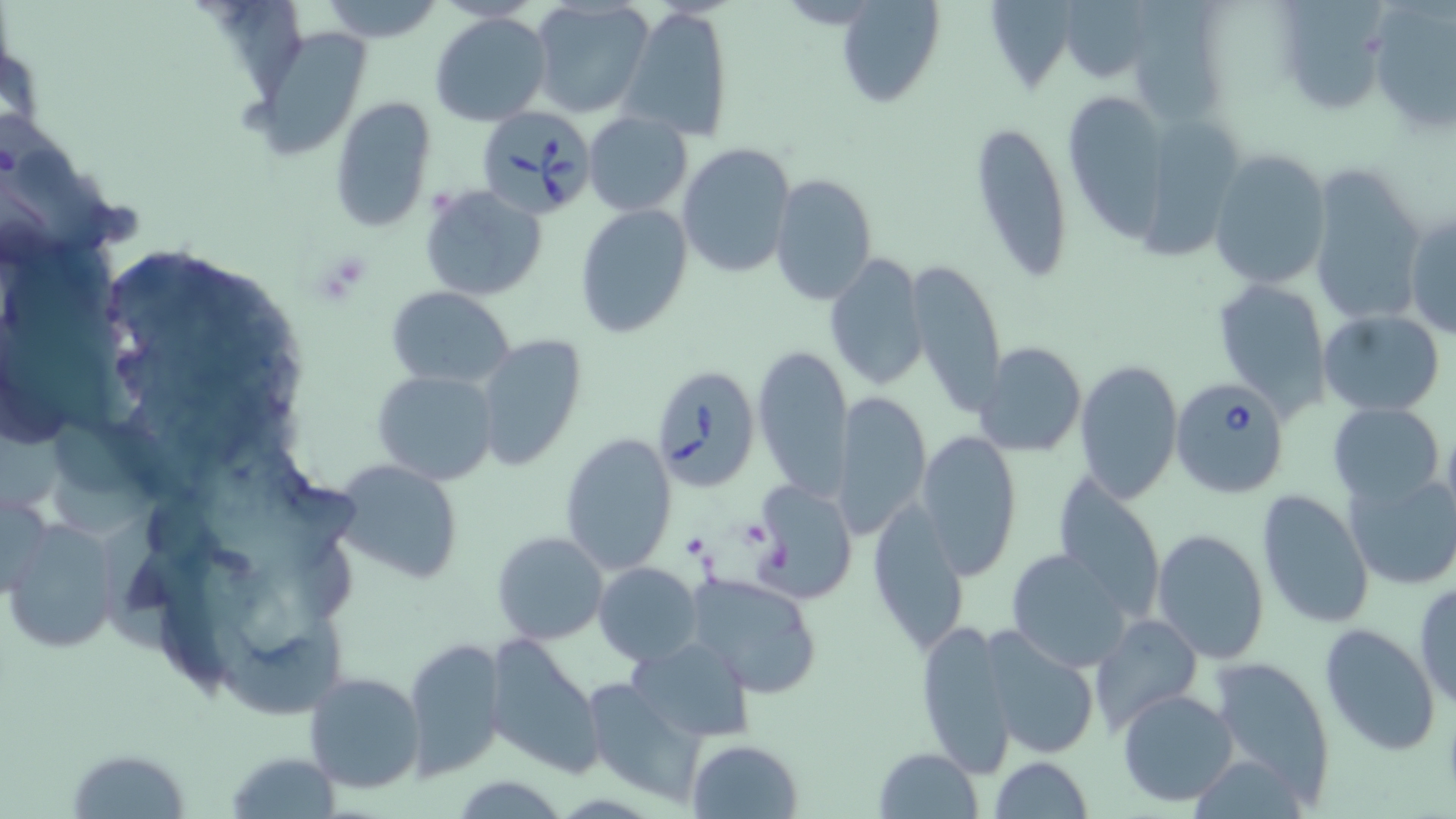

Summary:
  - Coordinate format: approximate bounding boxes as named x1/y1/x2/y2 corners in pixels
  - Platelet locations: (x1=736, y1=517, x2=772, y2=549), (x1=682, y1=531, x2=710, y2=559)
  - Uninfected red blood cell locations: (x1=316, y1=0, x2=445, y2=41), (x1=1057, y1=0, x2=1158, y2=84), (x1=834, y1=1, x2=942, y2=108), (x1=1366, y1=1, x2=1456, y2=133), (x1=528, y1=2, x2=651, y2=120), (x1=622, y1=6, x2=734, y2=140), (x1=430, y1=11, x2=553, y2=126), (x1=241, y1=25, x2=376, y2=163), (x1=1064, y1=92, x2=1170, y2=239), (x1=330, y1=96, x2=438, y2=233), (x1=584, y1=111, x2=695, y2=218), (x1=1139, y1=116, x2=1247, y2=258), (x1=970, y1=117, x2=1074, y2=285), (x1=678, y1=143, x2=796, y2=281), (x1=1206, y1=148, x2=1332, y2=291), (x1=1305, y1=167, x2=1427, y2=332), (x1=770, y1=175, x2=878, y2=304), (x1=420, y1=186, x2=548, y2=299), (x1=576, y1=205, x2=692, y2=338), (x1=1405, y1=210, x2=1456, y2=340), (x1=825, y1=252, x2=930, y2=394), (x1=906, y1=258, x2=1006, y2=415), (x1=1215, y1=276, x2=1331, y2=412), (x1=385, y1=286, x2=515, y2=388), (x1=1318, y1=310, x2=1445, y2=416), (x1=476, y1=336, x2=589, y2=474), (x1=975, y1=341, x2=1087, y2=457), (x1=753, y1=343, x2=853, y2=499), (x1=1074, y1=357, x2=1184, y2=504), (x1=371, y1=370, x2=499, y2=486), (x1=834, y1=390, x2=929, y2=541), (x1=1329, y1=402, x2=1444, y2=511), (x1=1440, y1=414, x2=1456, y2=537), (x1=916, y1=429, x2=1023, y2=579), (x1=558, y1=431, x2=679, y2=576), (x1=329, y1=458, x2=466, y2=585), (x1=1051, y1=470, x2=1166, y2=621), (x1=1344, y1=471, x2=1456, y2=591), (x1=755, y1=481, x2=857, y2=603), (x1=0, y1=486, x2=56, y2=606), (x1=1256, y1=489, x2=1375, y2=630), (x1=866, y1=498, x2=971, y2=653), (x1=4, y1=519, x2=123, y2=653), (x1=1152, y1=528, x2=1270, y2=663), (x1=492, y1=529, x2=609, y2=645), (x1=1006, y1=547, x2=1133, y2=671), (x1=595, y1=562, x2=703, y2=667), (x1=685, y1=571, x2=823, y2=697), (x1=1413, y1=579, x2=1455, y2=710), (x1=1088, y1=612, x2=1204, y2=738), (x1=916, y1=618, x2=1017, y2=777), (x1=1318, y1=623, x2=1441, y2=757), (x1=978, y1=625, x2=1102, y2=758), (x1=482, y1=635, x2=604, y2=776), (x1=626, y1=637, x2=755, y2=741), (x1=405, y1=639, x2=509, y2=778), (x1=1209, y1=654, x2=1335, y2=800), (x1=302, y1=671, x2=426, y2=794), (x1=579, y1=676, x2=705, y2=804), (x1=1116, y1=688, x2=1239, y2=806), (x1=687, y1=739, x2=803, y2=819), (x1=67, y1=747, x2=193, y2=819), (x1=873, y1=747, x2=983, y2=819), (x1=224, y1=751, x2=341, y2=818), (x1=990, y1=755, x2=1093, y2=819), (x1=1190, y1=755, x2=1310, y2=817)
  - Babesia divergens-infected red blood cell locations: (x1=479, y1=106, x2=600, y2=220), (x1=651, y1=364, x2=761, y2=491), (x1=1170, y1=376, x2=1288, y2=499)
  - Slide-level diagnosis: Babesia divergens
  - Magnification: 1000x
  - Image size: 1456×819 pixels
  - Stain: May-Grünwald-Giemsa
  - Field of view: single
  - Preparation: thin blood film
  - Modality: optical microscopy